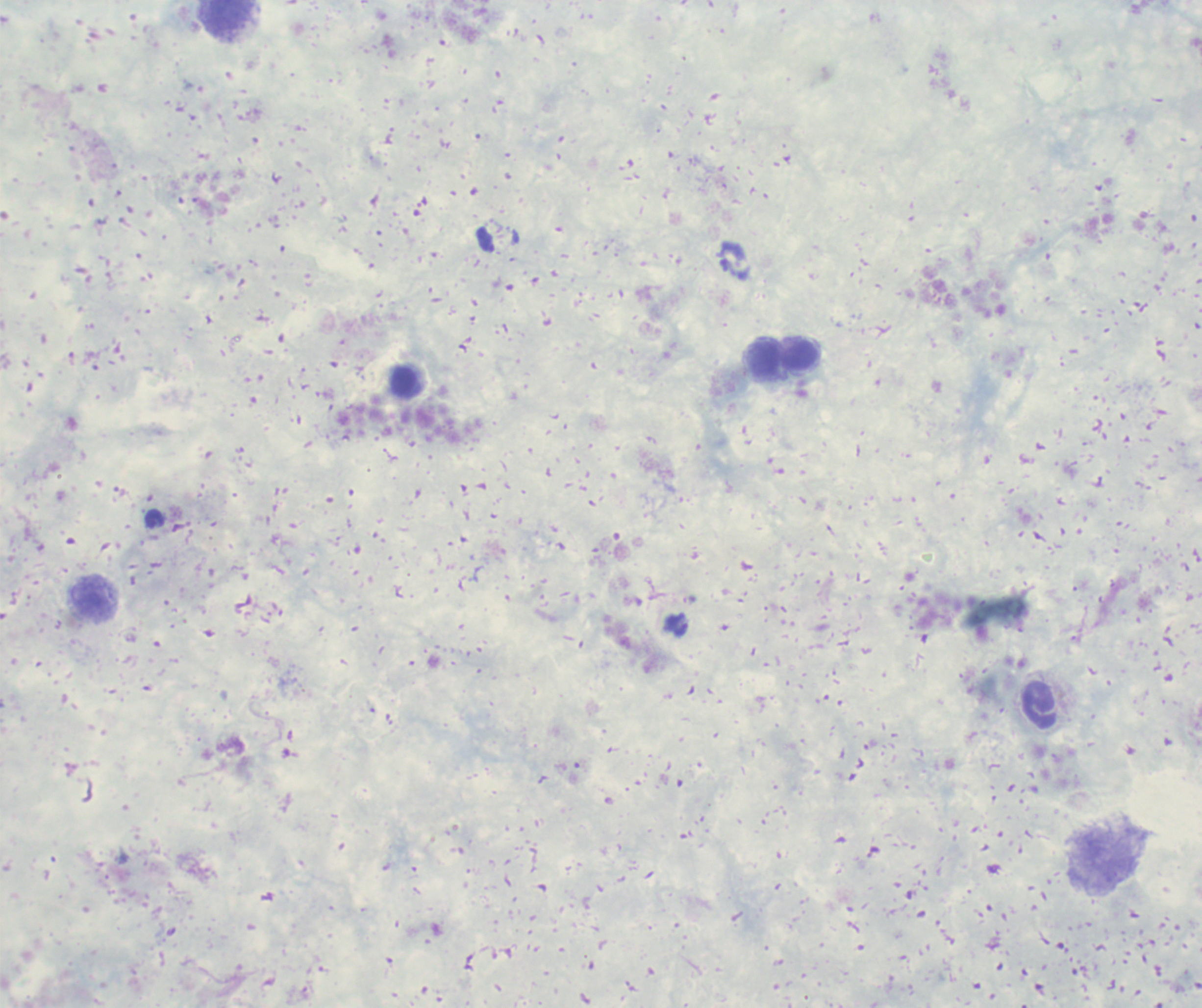

coordinate format = approximate centers as {x, y} in pixels
trophozoite locations = {677, 624}
leukocyte locations = {228, 17}, {800, 355}, {763, 356}, {403, 382}, {92, 596}, {1040, 705}
result = positive for Plasmodium parasites
image size = 1202×1008 pixels
context = previously used in an actual diagnosis
magnification = 100x
field of view = single
background quality = poor
stain = Romanowsky
preparation = thick blood film